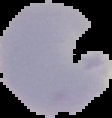 From a thin blood film. Segmented cell region on a black background. Result: no malaria parasites detected. Image is 112×118 pixels.